Identify the blood parasite species.
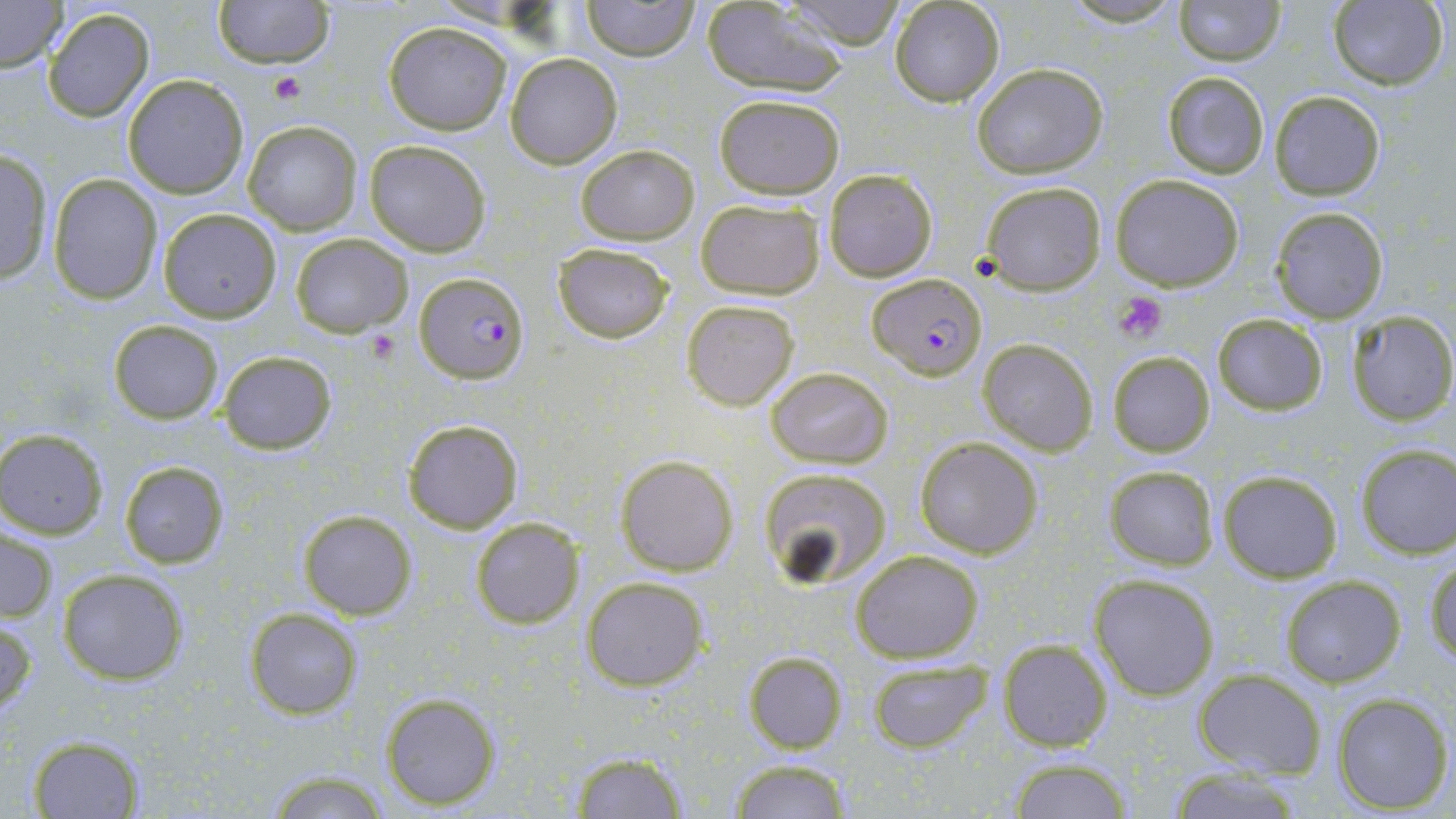
Plasmodium falciparum.

modality = light microscopy
Plasmodium falciparum-infected red blood cell locations = approximate bounding boxes as named x1/y1/x2/y2 corners in pixels: (x1=415, y1=273, x2=530, y2=384), (x1=868, y1=273, x2=985, y2=381)
image size = 1456×819 pixels
field of view = one of a larger specimen
platelet locations = approximate bounding boxes as named x1/y1/x2/y2 corners in pixels: (x1=268, y1=69, x2=307, y2=105), (x1=1114, y1=291, x2=1168, y2=343), (x1=361, y1=329, x2=401, y2=365)
preparation = thin blood film
magnification = 1000x
stain = May-Grünwald-Giemsa
uninfected red blood cell locations = approximate bounding boxes as named x1/y1/x2/y2 corners in pixels: (x1=0, y1=0, x2=69, y2=72), (x1=213, y1=0, x2=334, y2=68), (x1=580, y1=0, x2=701, y2=60), (x1=787, y1=0, x2=911, y2=49), (x1=890, y1=0, x2=1004, y2=106), (x1=1169, y1=0, x2=1286, y2=65), (x1=1327, y1=1, x2=1448, y2=90), (x1=700, y1=2, x2=848, y2=95), (x1=43, y1=7, x2=156, y2=124), (x1=383, y1=21, x2=512, y2=134), (x1=504, y1=53, x2=623, y2=169), (x1=972, y1=62, x2=1108, y2=178), (x1=1162, y1=70, x2=1270, y2=178), (x1=123, y1=75, x2=248, y2=198), (x1=1269, y1=91, x2=1386, y2=200), (x1=714, y1=94, x2=845, y2=199), (x1=242, y1=120, x2=361, y2=234), (x1=364, y1=137, x2=491, y2=256), (x1=574, y1=144, x2=699, y2=243), (x1=0, y1=149, x2=53, y2=283), (x1=823, y1=169, x2=937, y2=282), (x1=49, y1=173, x2=163, y2=304), (x1=1110, y1=173, x2=1245, y2=292), (x1=978, y1=180, x2=1108, y2=294), (x1=695, y1=198, x2=825, y2=300), (x1=1270, y1=205, x2=1389, y2=323), (x1=157, y1=207, x2=283, y2=322), (x1=289, y1=233, x2=412, y2=338), (x1=553, y1=242, x2=674, y2=345), (x1=680, y1=298, x2=800, y2=410), (x1=1345, y1=312, x2=1456, y2=425), (x1=1211, y1=313, x2=1328, y2=417), (x1=108, y1=320, x2=223, y2=423), (x1=979, y1=338, x2=1098, y2=456), (x1=217, y1=350, x2=338, y2=455), (x1=1106, y1=350, x2=1216, y2=459), (x1=764, y1=364, x2=895, y2=470), (x1=401, y1=418, x2=524, y2=533), (x1=0, y1=429, x2=109, y2=537), (x1=914, y1=437, x2=1042, y2=560), (x1=1353, y1=443, x2=1456, y2=559), (x1=615, y1=454, x2=738, y2=575), (x1=118, y1=459, x2=229, y2=570), (x1=1103, y1=465, x2=1221, y2=570), (x1=757, y1=466, x2=893, y2=585), (x1=1216, y1=469, x2=1344, y2=583), (x1=296, y1=508, x2=416, y2=620), (x1=469, y1=518, x2=584, y2=630), (x1=0, y1=524, x2=58, y2=625), (x1=850, y1=549, x2=984, y2=664), (x1=1426, y1=558, x2=1456, y2=667), (x1=57, y1=567, x2=190, y2=684), (x1=1089, y1=573, x2=1219, y2=700), (x1=580, y1=574, x2=709, y2=692), (x1=1279, y1=574, x2=1406, y2=688), (x1=244, y1=608, x2=363, y2=718), (x1=1, y1=614, x2=36, y2=718), (x1=997, y1=638, x2=1114, y2=752), (x1=742, y1=650, x2=849, y2=755), (x1=867, y1=659, x2=992, y2=750), (x1=1192, y1=669, x2=1326, y2=778), (x1=379, y1=690, x2=504, y2=809), (x1=1331, y1=694, x2=1452, y2=812), (x1=26, y1=734, x2=144, y2=817), (x1=569, y1=749, x2=691, y2=818), (x1=1007, y1=757, x2=1134, y2=818), (x1=725, y1=761, x2=857, y2=817), (x1=1161, y1=767, x2=1309, y2=818), (x1=264, y1=768, x2=392, y2=818)